Classify this cell by malaria status.
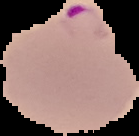

It is parasitized.

Summary:
  - Image type: cell region segmented out of the field of view; surrounding area masked to black
  - Preparation: thin blood smear
  - Image size: 139×136 pixels